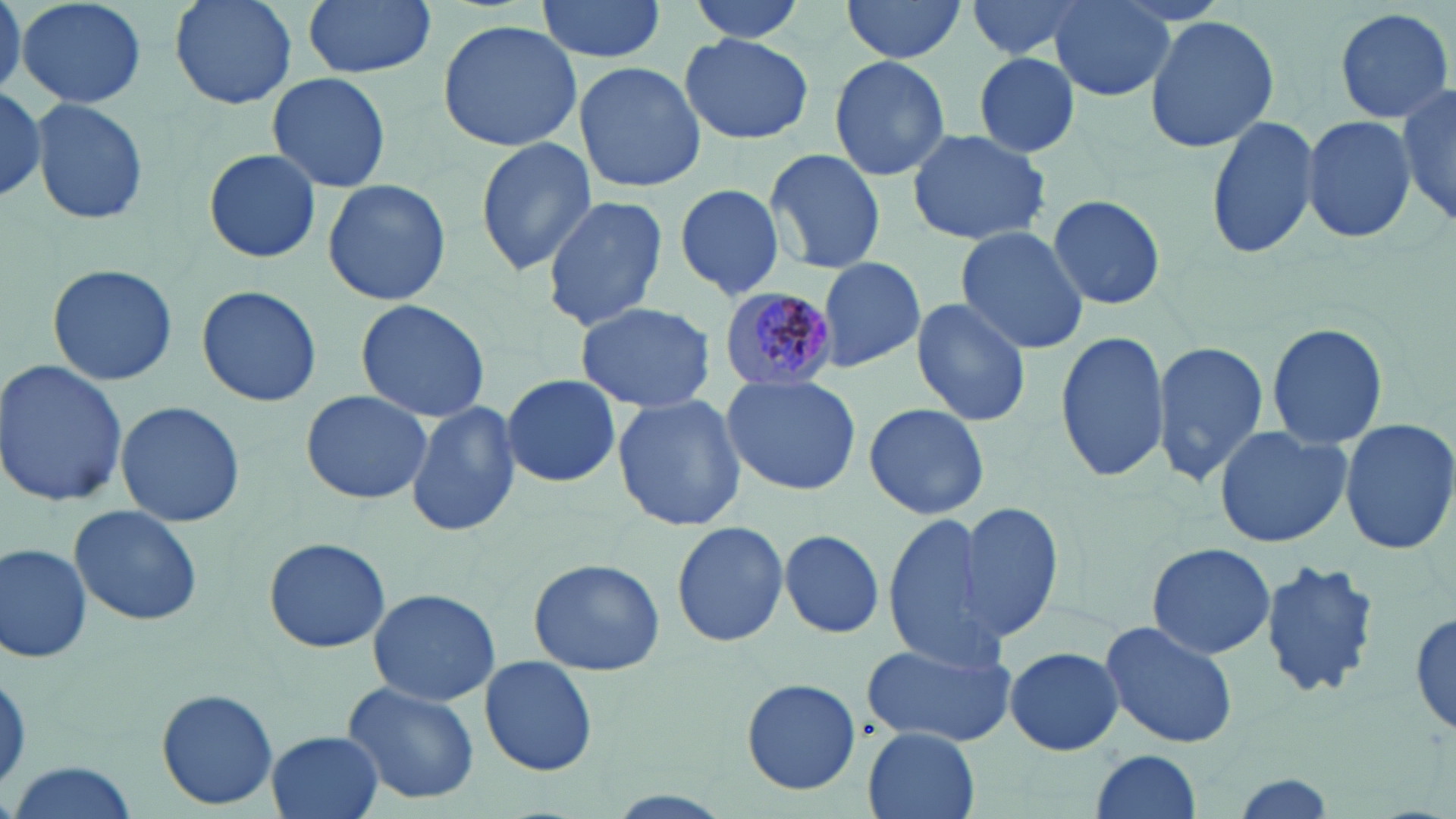 Approximate bounding boxes as (x1, y1, x2, y2) in pixels. Uninfected red blood cell locations: (0, 0, 23, 98), (16, 0, 148, 110), (166, 0, 301, 110), (302, 0, 435, 79), (534, 0, 666, 63), (686, 0, 809, 44), (841, 0, 968, 67), (964, 0, 1100, 62), (1048, 1, 1174, 102), (1333, 5, 1454, 125), (1142, 14, 1280, 153), (438, 19, 585, 152), (679, 31, 813, 145), (972, 51, 1081, 159), (828, 54, 951, 181), (573, 60, 706, 194), (266, 71, 392, 193), (0, 80, 47, 207), (1399, 83, 1456, 230), (30, 97, 149, 227), (1301, 113, 1418, 245), (1206, 114, 1322, 258), (905, 127, 1050, 247), (476, 136, 596, 274), (202, 146, 323, 265), (765, 147, 885, 274), (322, 177, 451, 307), (676, 183, 788, 302), (542, 195, 668, 331), (1046, 195, 1170, 311), (955, 226, 1092, 355), (813, 258, 926, 373), (47, 263, 179, 387), (194, 284, 323, 407), (355, 298, 491, 424), (911, 298, 1033, 427), (573, 301, 718, 414), (1265, 321, 1389, 452), (1054, 328, 1171, 483), (1149, 340, 1270, 490), (0, 357, 129, 510), (500, 374, 622, 489), (720, 374, 863, 496), (297, 389, 435, 508), (612, 394, 746, 532), (116, 400, 246, 527), (406, 400, 520, 538), (862, 403, 990, 519), (1341, 419, 1456, 554), (1212, 423, 1353, 547), (953, 499, 1067, 645), (71, 504, 202, 626), (882, 511, 1000, 664), (671, 521, 790, 648), (776, 528, 888, 642), (261, 536, 392, 653), (1, 542, 92, 664), (1146, 542, 1277, 658), (528, 558, 663, 677), (1257, 559, 1381, 699), (367, 587, 500, 707), (1409, 606, 1456, 741), (1099, 619, 1239, 751), (861, 635, 1017, 749), (1000, 646, 1129, 755), (479, 656, 599, 775), (737, 677, 862, 794), (339, 682, 481, 807), (155, 687, 279, 812), (863, 728, 981, 819), (266, 732, 385, 819), (1087, 749, 1205, 819), (2, 762, 142, 819). Plasmodium malariae-infected red blood cell locations: (717, 288, 838, 392). Slide-level diagnosis: Plasmodium malariae. Thin blood film. Captured at 1000x magnification. One field of a larger specimen. Image is 1456×819 pixels. May-Grünwald-Giemsa stain. Light microscopy.